Assess this cell for malaria.
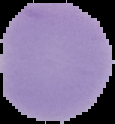
It is uninfected.

Cell region segmented out of the field of view; the surrounding area is masked to black. From a thin blood smear. Image is 115×124 pixels.